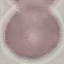
Summary:
  - Result: no malaria parasites seen
  - Image type: automatically extracted cell patch, resized to 64 × 64 pixels
  - Capture: smartphone through the microscope eyepiece
  - Stain: Giemsa
  - Preparation: thin blood smear